Report the malaria status of this cell.
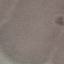

It is uninfected.

Giemsa stain. Automatically extracted cell patch, resized to 64 × 64 pixels. Photographed with a smartphone camera at the microscope eyepiece. Thin blood smear.